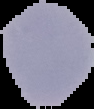

{
  "image_type": "cell region segmented out of the field of view; surrounding area masked to black",
  "preparation": "thin blood film",
  "image_size": "94×109 pixels",
  "result": "no malaria parasites detected"
}